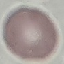 Malaria status: uninfected. Thin smear of blood. Automatically extracted cell patch, resized to 64 × 64 pixels. Giemsa-stained preparation. Acquired by smartphone through the microscope eyepiece.